Give the position of every malaria parasite and every leukocyte.
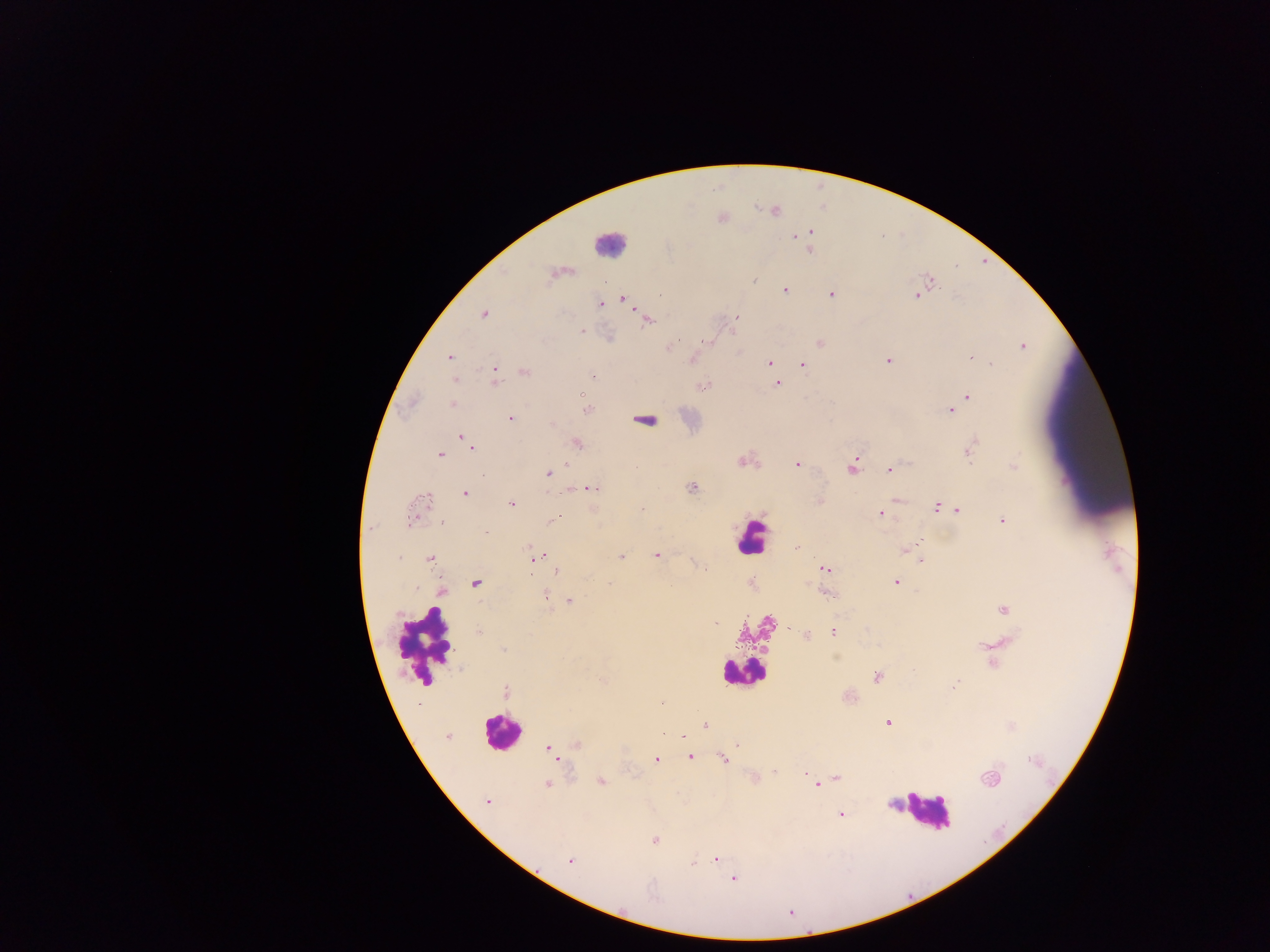

Approximate centers as (x, y) in pixels.
Malaria parasites: (775, 211), (810, 231), (796, 236), (809, 248), (565, 271), (553, 273), (755, 280), (931, 281), (784, 289), (831, 294), (915, 295), (623, 298), (600, 304), (484, 315), (737, 317), (648, 320), (581, 331), (677, 341), (709, 342), (819, 342), (670, 345), (1022, 346), (450, 357), (969, 358), (693, 360), (887, 361), (769, 363), (991, 363), (802, 365), (524, 372), (496, 373), (593, 376), (778, 384), (703, 386), (967, 397), (452, 404), (586, 410), (950, 410), (510, 419), (552, 425), (463, 438), (469, 443), (577, 444), (472, 448), (969, 452), (439, 454), (743, 461), (567, 464), (797, 465), (1014, 465), (851, 468), (890, 470), (549, 474), (692, 487), (592, 488), (465, 493), (427, 498), (896, 500), (819, 502), (511, 504), (935, 507), (643, 508), (948, 508), (957, 510), (880, 513), (1003, 520), (441, 521), (552, 521), (410, 522), (485, 532), (915, 545), (528, 548), (796, 548), (905, 550), (621, 556), (656, 556), (399, 557), (532, 558), (430, 559), (921, 561), (825, 569), (556, 571), (896, 582), (475, 583), (610, 585), (416, 587), (442, 591), (828, 592), (545, 595), (569, 600), (1004, 610), (716, 624), (833, 632), (479, 633), (806, 635), (503, 650), (877, 677), (602, 680), (954, 685), (506, 692), (888, 723), (706, 725), (447, 736), (683, 736), (737, 744), (576, 745), (549, 749), (689, 757), (723, 758), (657, 760), (774, 771), (805, 774), (837, 778), (810, 779), (991, 779), (600, 781), (815, 784), (547, 785), (488, 801), (840, 814), (655, 840), (715, 858), (569, 860), (694, 862), (733, 879), (654, 898), (790, 912).
Leukocytes (some below the resolvable threshold): (608, 242), (644, 418), (750, 537), (425, 644), (741, 672), (500, 731), (925, 811).

preparation = thick blood film
field of view = single
capture = mobile-phone photograph through a microscope
country = Ghana
image size = 1270×952 pixels